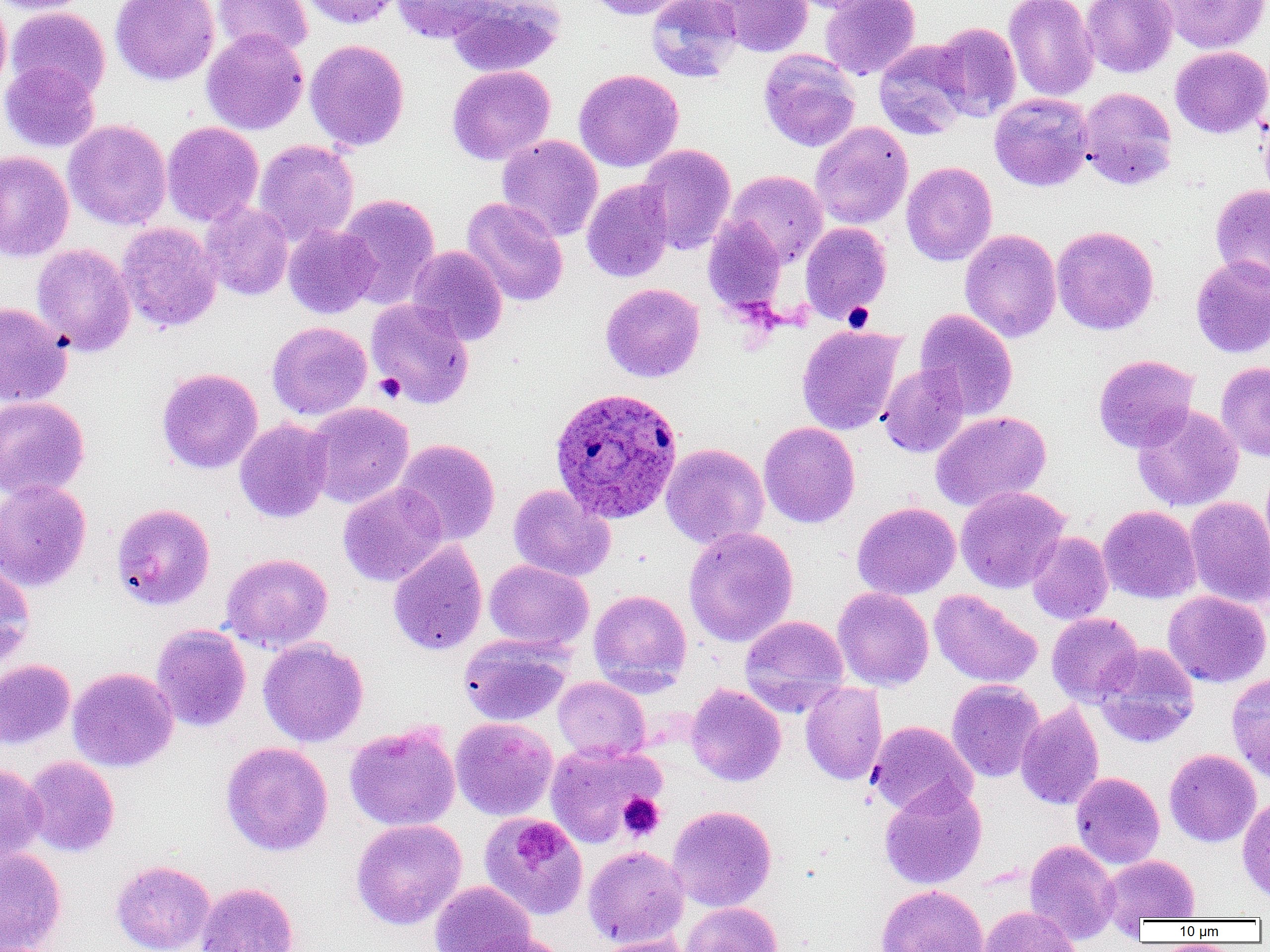

Summary:
  - Coordinate format: approximate bounding boxes as named x1/y1/x2/y2 corners in pixels
  - Platelet locations: (x1=843, y1=302, x2=874, y2=332), (x1=374, y1=373, x2=405, y2=403), (x1=618, y1=793, x2=665, y2=840)
  - Plasmodium ovale-infected red blood cell locations: (x1=550, y1=387, x2=685, y2=525)
  - Uninfected red blood cell locations: (x1=0, y1=0, x2=12, y2=100), (x1=0, y1=0, x2=93, y2=15), (x1=110, y1=0, x2=220, y2=85), (x1=213, y1=0, x2=313, y2=58), (x1=299, y1=0, x2=401, y2=29), (x1=392, y1=0, x2=497, y2=44), (x1=448, y1=0, x2=565, y2=77), (x1=587, y1=0, x2=695, y2=20), (x1=645, y1=0, x2=743, y2=83), (x1=712, y1=0, x2=814, y2=57), (x1=783, y1=0, x2=891, y2=13), (x1=820, y1=0, x2=921, y2=80), (x1=1003, y1=0, x2=1098, y2=102), (x1=1081, y1=0, x2=1178, y2=77), (x1=1159, y1=0, x2=1270, y2=54), (x1=6, y1=7, x2=110, y2=102), (x1=931, y1=22, x2=1021, y2=121), (x1=201, y1=28, x2=309, y2=135), (x1=305, y1=39, x2=410, y2=151), (x1=873, y1=40, x2=971, y2=140), (x1=1170, y1=46, x2=1270, y2=137), (x1=759, y1=49, x2=860, y2=151), (x1=0, y1=60, x2=100, y2=153), (x1=447, y1=65, x2=555, y2=165), (x1=574, y1=69, x2=683, y2=172), (x1=1078, y1=87, x2=1177, y2=190), (x1=989, y1=93, x2=1094, y2=191), (x1=63, y1=120, x2=172, y2=231), (x1=162, y1=121, x2=264, y2=227), (x1=810, y1=121, x2=913, y2=230), (x1=497, y1=134, x2=603, y2=241), (x1=253, y1=140, x2=359, y2=246), (x1=638, y1=144, x2=736, y2=255), (x1=0, y1=151, x2=74, y2=261), (x1=901, y1=161, x2=997, y2=266), (x1=724, y1=170, x2=828, y2=268), (x1=581, y1=179, x2=675, y2=283), (x1=1210, y1=184, x2=1270, y2=287), (x1=336, y1=193, x2=441, y2=310), (x1=461, y1=198, x2=568, y2=307), (x1=200, y1=200, x2=294, y2=301), (x1=703, y1=215, x2=787, y2=313), (x1=800, y1=221, x2=892, y2=323), (x1=116, y1=222, x2=221, y2=332), (x1=283, y1=225, x2=378, y2=318), (x1=1051, y1=225, x2=1159, y2=335), (x1=959, y1=228, x2=1061, y2=343), (x1=31, y1=243, x2=135, y2=357), (x1=407, y1=246, x2=508, y2=346), (x1=1191, y1=255, x2=1270, y2=358), (x1=600, y1=283, x2=705, y2=383), (x1=366, y1=298, x2=475, y2=409), (x1=0, y1=302, x2=72, y2=407), (x1=915, y1=309, x2=1018, y2=420), (x1=267, y1=321, x2=372, y2=420), (x1=796, y1=324, x2=905, y2=435), (x1=1093, y1=354, x2=1199, y2=453), (x1=1216, y1=361, x2=1270, y2=461), (x1=877, y1=363, x2=969, y2=458), (x1=156, y1=368, x2=263, y2=473), (x1=0, y1=396, x2=90, y2=501), (x1=307, y1=402, x2=414, y2=509), (x1=1132, y1=404, x2=1243, y2=512), (x1=931, y1=411, x2=1051, y2=512), (x1=234, y1=419, x2=334, y2=523), (x1=758, y1=422, x2=860, y2=528), (x1=393, y1=439, x2=500, y2=545), (x1=661, y1=443, x2=769, y2=550), (x1=0, y1=480, x2=92, y2=592), (x1=338, y1=482, x2=447, y2=587), (x1=508, y1=485, x2=616, y2=582), (x1=956, y1=486, x2=1069, y2=593), (x1=1184, y1=495, x2=1270, y2=610), (x1=852, y1=501, x2=961, y2=600), (x1=111, y1=503, x2=215, y2=611), (x1=1098, y1=505, x2=1201, y2=603), (x1=683, y1=527, x2=798, y2=647), (x1=1026, y1=531, x2=1113, y2=625), (x1=387, y1=540, x2=488, y2=656), (x1=221, y1=553, x2=333, y2=652), (x1=484, y1=559, x2=593, y2=652), (x1=0, y1=564, x2=35, y2=667), (x1=833, y1=587, x2=934, y2=691), (x1=588, y1=589, x2=692, y2=693), (x1=929, y1=589, x2=1043, y2=688), (x1=1163, y1=591, x2=1270, y2=688), (x1=1046, y1=612, x2=1143, y2=705), (x1=740, y1=615, x2=849, y2=715), (x1=151, y1=624, x2=251, y2=732), (x1=458, y1=634, x2=572, y2=726), (x1=258, y1=637, x2=369, y2=747), (x1=1093, y1=643, x2=1200, y2=748), (x1=0, y1=659, x2=75, y2=749), (x1=68, y1=667, x2=179, y2=772), (x1=1226, y1=671, x2=1270, y2=783), (x1=553, y1=676, x2=651, y2=762), (x1=946, y1=679, x2=1045, y2=783), (x1=800, y1=681, x2=888, y2=785), (x1=686, y1=683, x2=786, y2=786), (x1=1016, y1=702, x2=1104, y2=810), (x1=451, y1=717, x2=558, y2=820), (x1=867, y1=721, x2=977, y2=817), (x1=344, y1=723, x2=461, y2=831), (x1=545, y1=740, x2=664, y2=847), (x1=220, y1=742, x2=333, y2=856), (x1=1164, y1=749, x2=1261, y2=847), (x1=22, y1=756, x2=120, y2=857), (x1=0, y1=764, x2=47, y2=863), (x1=1071, y1=772, x2=1165, y2=869), (x1=879, y1=781, x2=987, y2=889), (x1=1237, y1=793, x2=1270, y2=903), (x1=667, y1=805, x2=776, y2=911), (x1=479, y1=812, x2=589, y2=921), (x1=351, y1=819, x2=467, y2=929), (x1=1024, y1=839, x2=1121, y2=943), (x1=583, y1=845, x2=689, y2=948), (x1=0, y1=846, x2=67, y2=952), (x1=1099, y1=855, x2=1200, y2=926), (x1=110, y1=859, x2=216, y2=952), (x1=430, y1=880, x2=536, y2=952), (x1=195, y1=882, x2=300, y2=952), (x1=876, y1=884, x2=989, y2=952), (x1=680, y1=901, x2=783, y2=952), (x1=979, y1=905, x2=1082, y2=952), (x1=466, y1=932, x2=572, y2=952), (x1=592, y1=934, x2=693, y2=952)
  - Slide-level diagnosis: Plasmodium ovale
  - Magnification: 1000x
  - Modality: light microscopy
  - Preparation: thin blood smear
  - Image size: 1270×952 pixels
  - Field of view: single